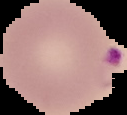

Summary:
  - Image size: 127×115 pixels
  - Preparation: thin blood film
  - Image type: segmented cell region on a black background
  - Result: malaria parasites identified